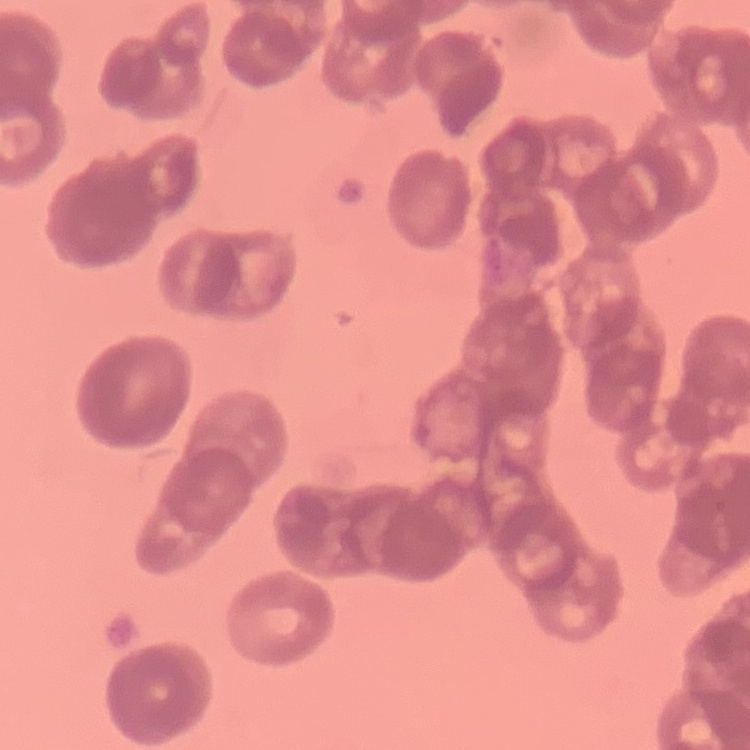
red blood cell morphology = rouleaux formation
preparation = thin peripheral smear
stain = Field's or Giemsa
image type = square crop of a larger photomicrograph